Report the malaria status of this cell.
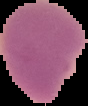

Uninfected.

Image is 88×106 pixels. From a thin blood smear. The area outside the segmented cell region is set to black.